Outline each blood parasite and name the species.
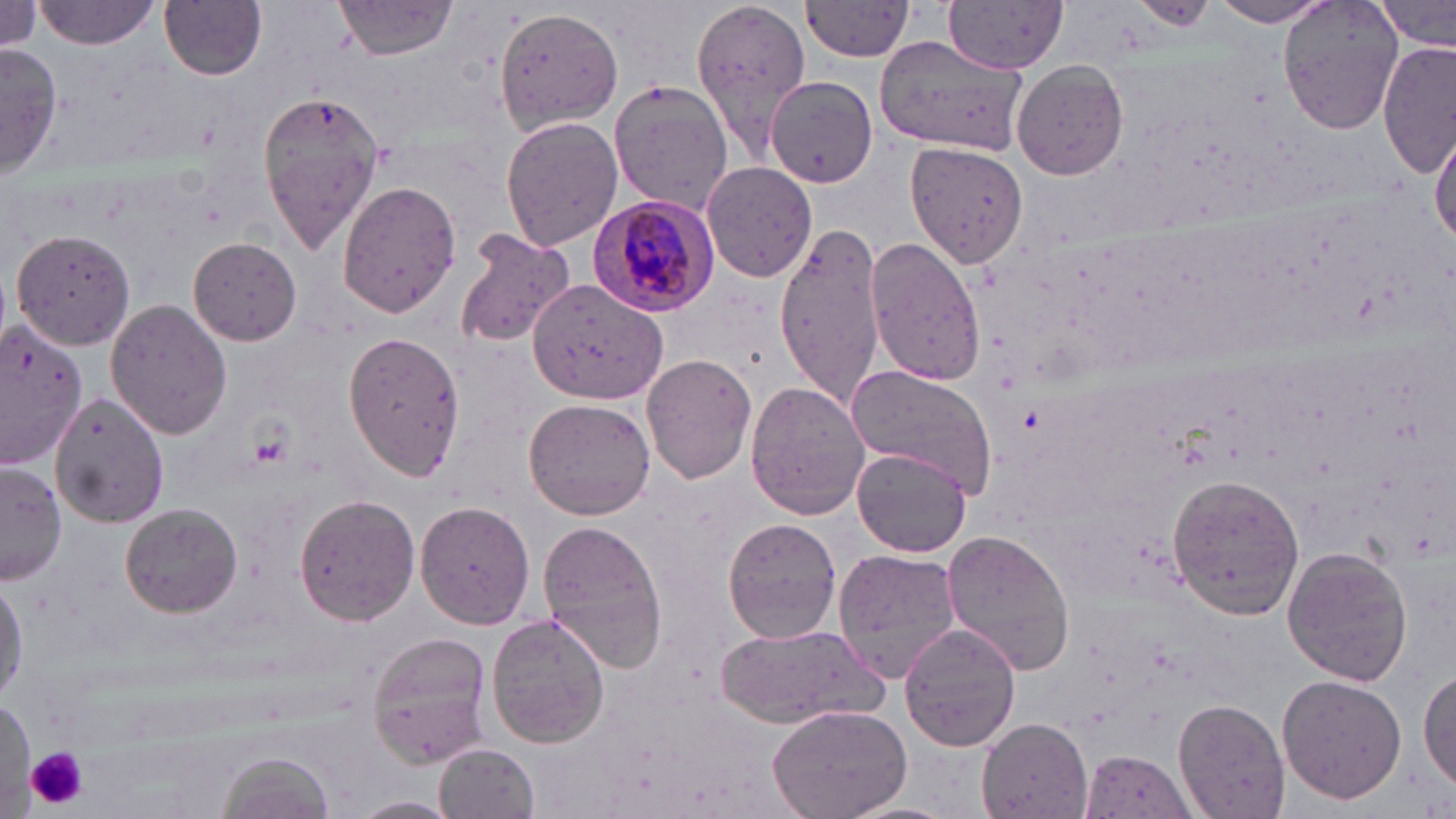
Approximate bounding boxes as (x1, y1, x2, y2) in pixels.
Plasmodium malariae-infected red blood cells: (590, 193, 722, 317).
No Plasmodium falciparum, Plasmodium ovale, Plasmodium vivax, Babesia divergens, or Trypanosoma brucei observed.

Platelet locations: (27, 746, 88, 807). Uninfected red blood cell locations: (160, 0, 268, 80), (335, 0, 461, 60), (689, 0, 810, 158), (947, 0, 1069, 72), (1128, 0, 1219, 33), (1278, 0, 1404, 137), (1379, 0, 1454, 53), (0, 1, 51, 54), (37, 1, 158, 49), (1207, 1, 1334, 26), (802, 2, 918, 62), (494, 5, 623, 134), (877, 36, 1028, 154), (1379, 40, 1455, 175), (1, 44, 61, 176), (1012, 61, 1130, 180), (764, 76, 877, 187), (608, 79, 734, 213), (256, 88, 385, 255), (499, 114, 621, 251), (1431, 128, 1455, 244), (904, 141, 1030, 269), (701, 162, 816, 283), (337, 180, 461, 320), (772, 222, 886, 409), (452, 228, 574, 350), (12, 229, 138, 351), (865, 236, 987, 388), (188, 237, 303, 345), (528, 279, 666, 404), (105, 300, 232, 439), (0, 321, 84, 467), (344, 331, 466, 480), (642, 353, 758, 485), (845, 364, 999, 501), (746, 382, 871, 520), (49, 392, 170, 527), (524, 397, 655, 520), (853, 448, 971, 557), (0, 465, 65, 587), (1166, 473, 1306, 620), (292, 494, 418, 625), (417, 500, 534, 629), (120, 503, 243, 616), (721, 516, 842, 643), (538, 519, 669, 673), (942, 527, 1077, 676), (1282, 545, 1413, 687), (833, 549, 959, 684), (0, 574, 26, 707), (488, 613, 610, 749), (715, 623, 885, 729), (899, 625, 1021, 751), (367, 633, 492, 765), (1420, 665, 1456, 790), (1276, 674, 1407, 805), (2, 695, 35, 808), (1174, 698, 1291, 819), (766, 706, 912, 819), (977, 719, 1092, 816), (434, 744, 539, 819), (1081, 748, 1197, 817), (217, 751, 334, 819), (352, 795, 461, 817). Slide-level diagnosis: Plasmodium malariae. May-Grünwald-Giemsa-stained preparation. Image is 1456×819 pixels. Light microscopy. One field of a larger specimen. Captured at 1000x magnification. Thin blood film.